Comment on the morphology of the red blood cells.
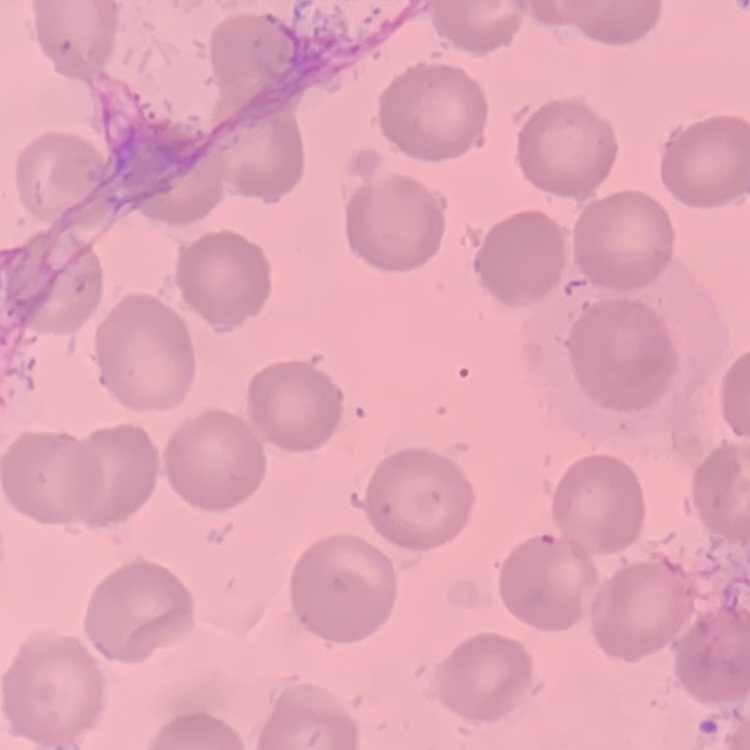
They show no rouleaux formation.

Summary:
  - Stain: Field's or Giemsa
  - Image type: square crop of a larger photomicrograph
  - Preparation: thin peripheral smear